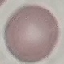

Summary:
  - Result: negative for malaria parasites
  - Capture: smartphone camera at the microscope eyepiece
  - Preparation: thin blood smear
  - Image type: cell patch, automatically extracted from a larger field of view and resized to 64 × 64 pixels
  - Stain: Giemsa